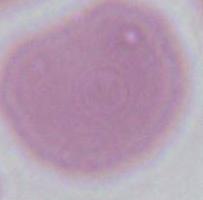
{
  "modality": "photomicrograph",
  "magnification": "1000x",
  "identification": "red blood cell"
}